Identify the cell.
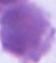
An erythrocyte.

Summary:
  - Modality: photomicrograph
  - Magnification: 1000x